Point out each leukocyte.
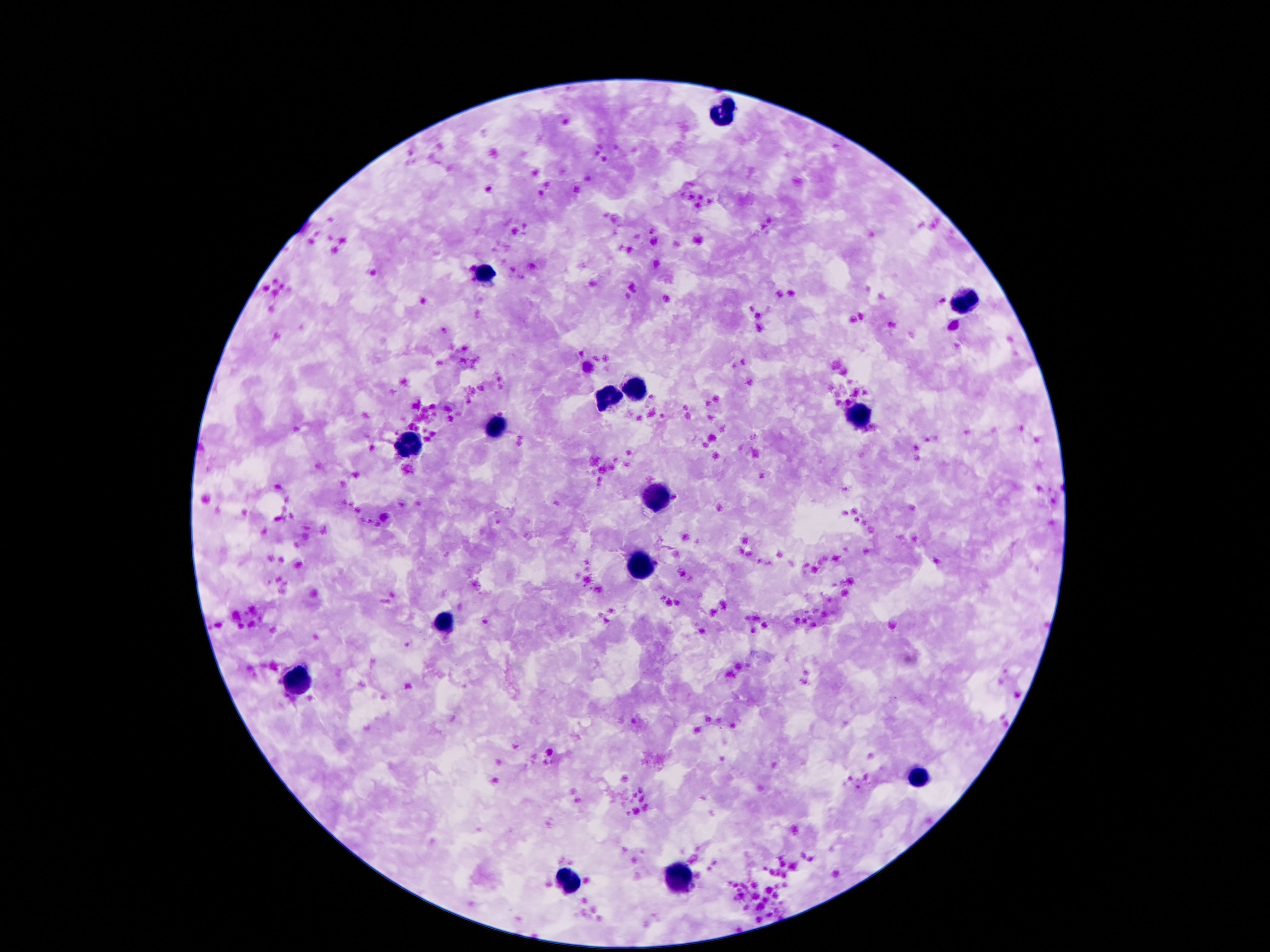
Approximate centers as {x, y} in pixels.
Leukocytes: {726, 109}, {480, 274}, {965, 303}, {635, 389}, {609, 399}, {859, 416}, {494, 428}, {410, 445}, {658, 495}, {642, 565}, {443, 623}, {299, 680}, {916, 778}, {680, 879}, {568, 880}.

magnification = 100x
field of view = one from this slide
image size = 1270×952 pixels
stain = Giemsa
preparation = thick blood film
patient malaria status = not infected
capture = smartphone camera through the microscope eyepiece